Give the extent of all Plasmodium falciparum-infected red blood cells.
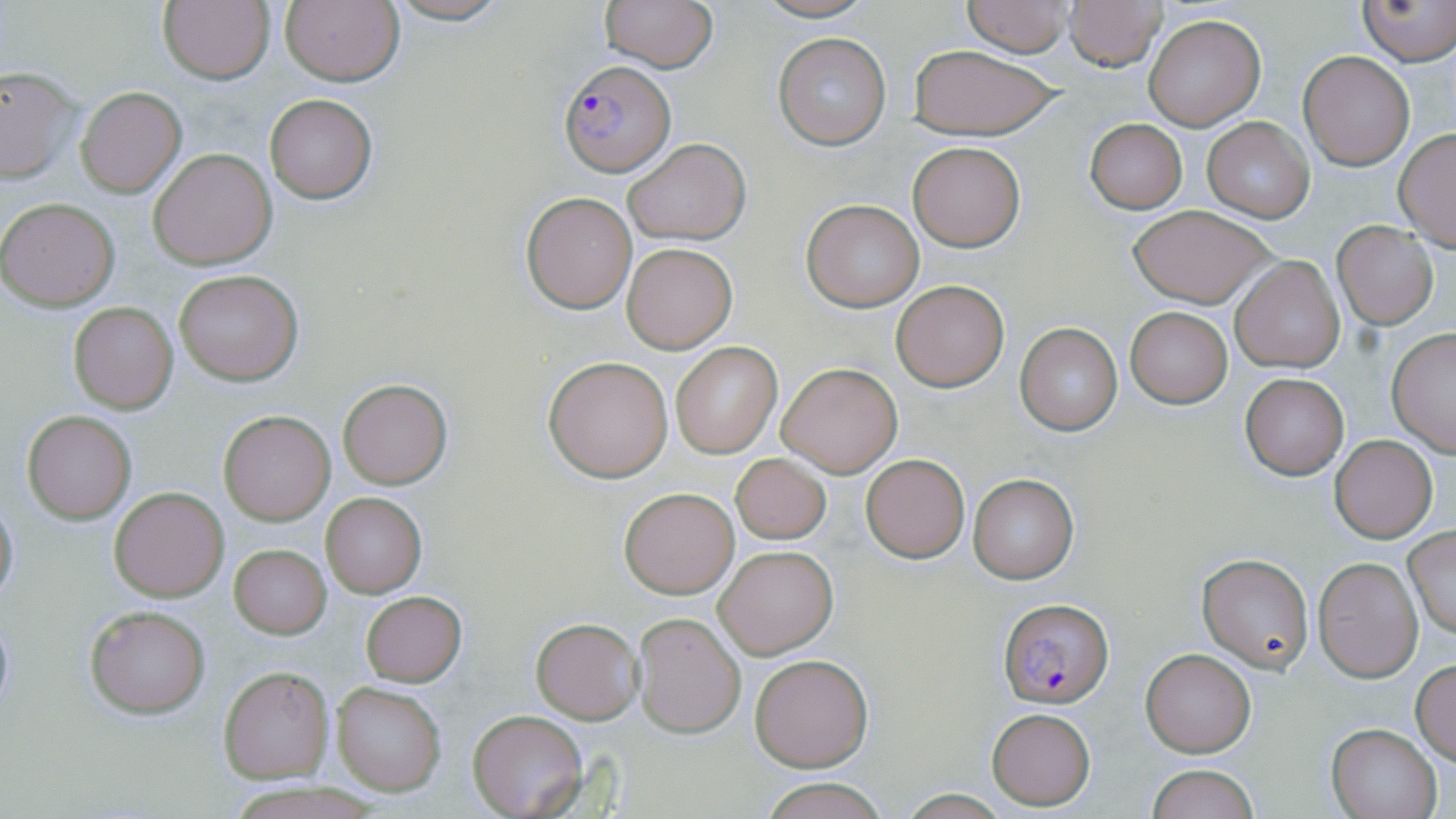

Approximate bounding boxes as [x1, y1, x2, y2] in pixels.
Plasmodium falciparum-infected red blood cells: [559, 61, 677, 176], [998, 599, 1113, 710].

Uninfected red blood cell locations: [157, 0, 275, 85], [382, 0, 515, 25], [598, 0, 721, 72], [749, 0, 878, 23], [1357, 0, 1455, 65], [961, 1, 1076, 56], [1063, 1, 1167, 72], [280, 2, 404, 86], [1143, 15, 1265, 130], [773, 31, 892, 151], [905, 45, 1066, 140], [1298, 51, 1414, 170], [0, 64, 80, 184], [76, 86, 186, 197], [263, 94, 378, 203], [1201, 116, 1314, 222], [1084, 118, 1188, 214], [1394, 129, 1456, 251], [622, 139, 749, 245], [908, 142, 1025, 251], [148, 149, 276, 270], [520, 191, 638, 313], [0, 198, 119, 310], [801, 199, 925, 312], [1128, 203, 1274, 308], [1333, 222, 1439, 329], [622, 243, 737, 353], [1231, 256, 1344, 373], [174, 271, 304, 386], [891, 280, 1009, 391], [69, 301, 178, 413], [1125, 307, 1231, 408], [1015, 323, 1122, 435], [1386, 328, 1456, 456], [670, 341, 783, 458], [543, 355, 676, 482], [777, 361, 903, 477], [1240, 372, 1349, 480], [337, 379, 451, 489], [219, 410, 334, 525], [22, 411, 135, 523], [1330, 435, 1438, 543], [861, 454, 968, 563], [729, 455, 831, 544], [967, 473, 1078, 583], [618, 486, 739, 598], [109, 487, 229, 601], [322, 491, 425, 597], [0, 494, 19, 610], [1403, 526, 1455, 639], [713, 543, 837, 660], [229, 544, 331, 638], [1196, 553, 1315, 674], [1314, 557, 1423, 682], [359, 590, 465, 685], [85, 605, 211, 718], [632, 610, 746, 738], [531, 616, 644, 724], [1142, 649, 1256, 757], [749, 653, 873, 772], [1411, 658, 1456, 764], [219, 666, 334, 781], [332, 681, 446, 795], [987, 708, 1096, 809], [469, 710, 588, 818], [1326, 723, 1442, 819], [1147, 764, 1259, 819], [759, 779, 891, 819], [225, 783, 382, 819]. Slide-level diagnosis: Plasmodium falciparum. Single field of view. Light microscopy. May-Grünwald-Giemsa stain. Captured at 1000x magnification. Image is 1456×819 pixels. Thin blood smear.